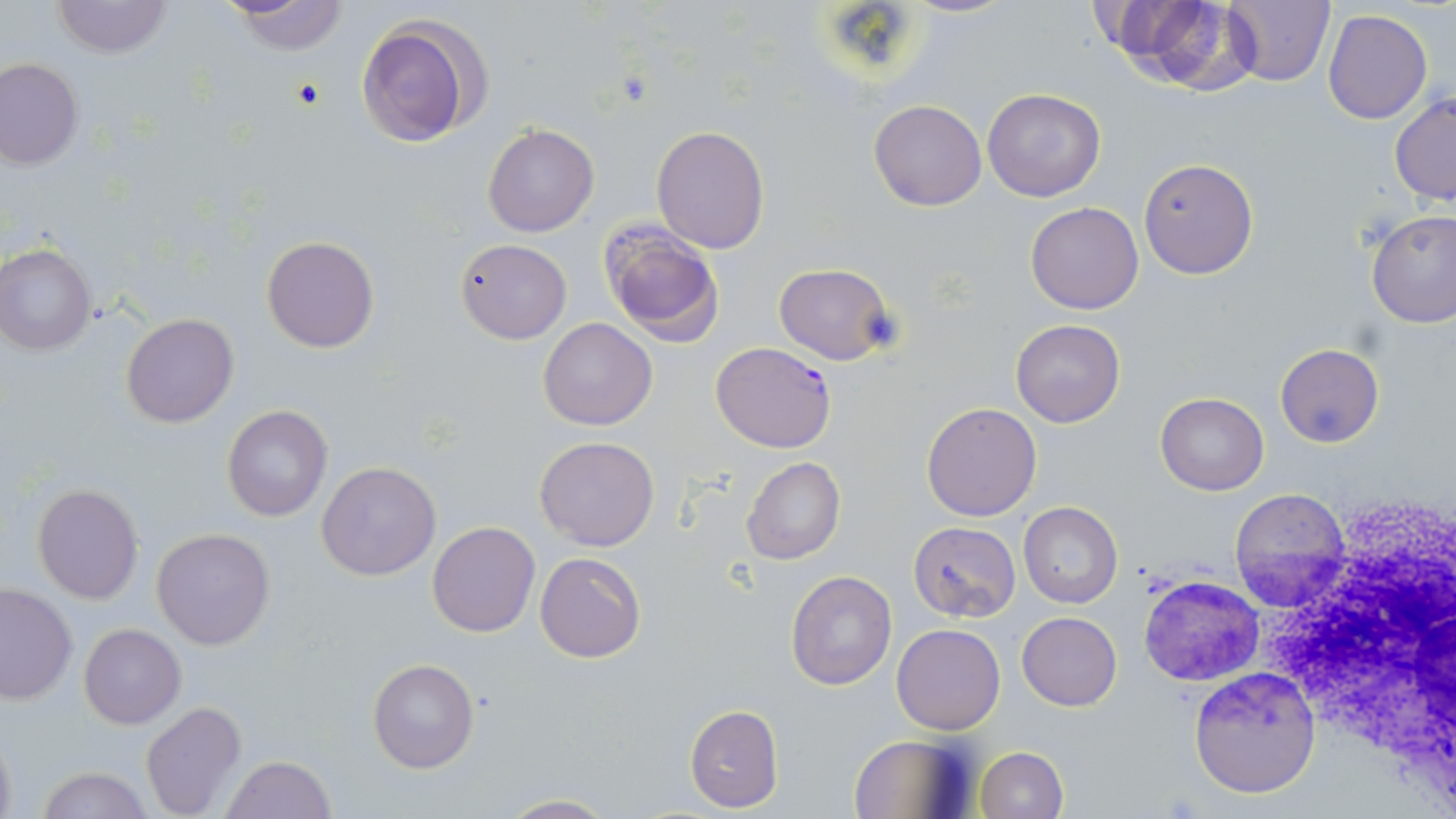
{
  "slide_level_diagnosis": "Plasmodium falciparum",
  "white_blood_cell_locations": "approximate bounding boxes as (x1, y1, x2, y2) in pixels: (1255, 494, 1456, 774)",
  "plasmodium_falciparum_infected_red_blood_cell_locations": "approximate bounding boxes as (x1, y1, x2, y2) in pixels: (711, 342, 836, 453)",
  "modality": "optical microscopy",
  "image_size": "1456×819 pixels",
  "preparation": "thin blood smear",
  "magnification": "1000x",
  "stain": "May-Grünwald-Giemsa",
  "uninfected_red_blood_cell_locations": "approximate bounding boxes as (x1, y1, x2, y2) in pixels: (901, 0, 1014, 17), (1224, 0, 1336, 86), (51, 1, 172, 58), (222, 1, 350, 55), (1102, 1, 1255, 91), (1323, 10, 1433, 124), (356, 13, 488, 147), (1, 59, 84, 169), (982, 88, 1106, 202), (1390, 92, 1456, 204), (868, 99, 986, 210), (482, 124, 598, 237), (650, 126, 769, 253), (1138, 157, 1259, 280), (1025, 202, 1143, 314), (1366, 209, 1456, 328), (599, 221, 727, 346), (261, 235, 379, 353), (455, 238, 571, 344), (0, 245, 97, 354), (773, 263, 897, 365), (120, 313, 238, 428), (539, 317, 657, 431), (1010, 319, 1126, 428), (1275, 343, 1384, 448), (1155, 392, 1269, 494), (919, 402, 1042, 521), (221, 404, 333, 523), (534, 436, 659, 551), (741, 457, 845, 566), (318, 461, 440, 582), (32, 484, 143, 604), (1229, 488, 1353, 611), (1018, 502, 1123, 607), (427, 521, 540, 637), (909, 521, 1021, 622), (152, 527, 274, 649), (535, 552, 645, 662), (785, 571, 897, 691), (1138, 573, 1264, 688), (1, 583, 77, 705), (1017, 612, 1122, 710), (79, 624, 186, 730), (893, 624, 1005, 734), (367, 657, 479, 774), (1188, 666, 1321, 798), (140, 702, 246, 819), (683, 703, 783, 812), (0, 727, 17, 819), (848, 732, 977, 818), (974, 746, 1069, 819), (220, 756, 337, 818), (34, 765, 152, 819), (494, 794, 620, 818)",
  "field_of_view": "single"
}